Identify the parasite.
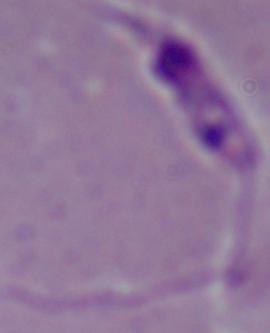
Leishmania.

Photomicrograph. Captured at 1000x magnification.